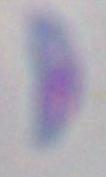 Micrograph. Captured at 1000x magnification. Toxoplasma gondii is shown.